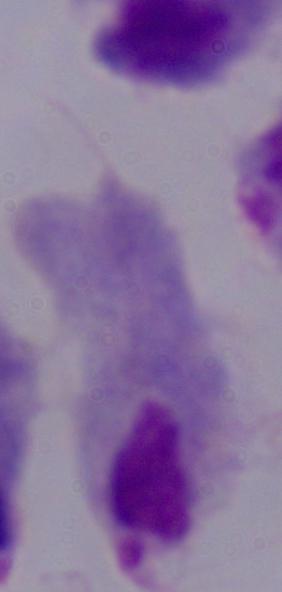

1000x magnification. Micrograph. A trichomonad is shown.